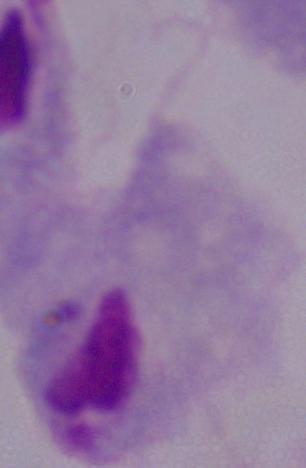
magnification = 1000x
modality = photomicrograph
identification = trichomonad